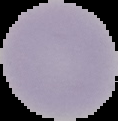

result: negative for Plasmodium parasites
image_type: segmented cell region on a black background
preparation: thin blood smear
image_size: 118×121 pixels